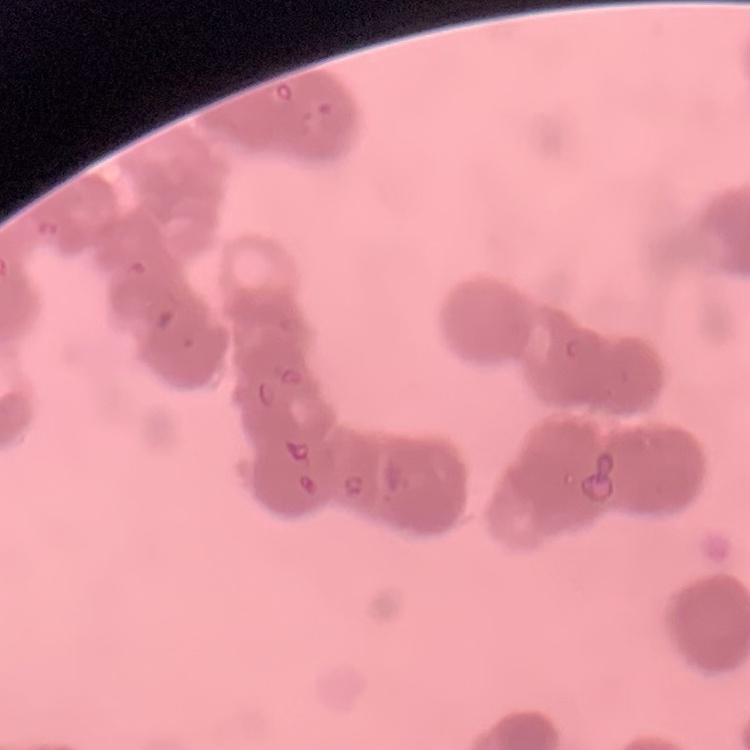
erythrocyte_morphology: rouleaux formation
preparation: thin blood film
stain: Field's or Giemsa
image_type: one tile cut from a larger photomicrograph